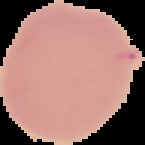

Summary:
  - Image size: 145×145 pixels
  - Result: no Plasmodium parasites seen
  - Image type: cell region segmented out of the field of view; surrounding area masked to black
  - Preparation: thin blood film